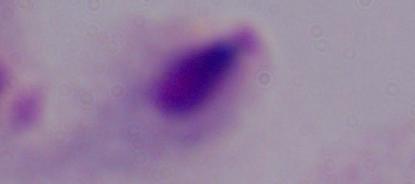 Micrograph. Captured at 1000x magnification. A trichomonad is seen.